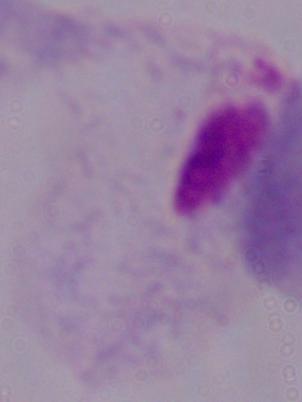
identification: trichomonad
modality: photomicrograph
magnification: 1000x